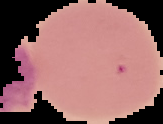
Image is 163×124 pixels. Malaria status: uninfected. The area outside the segmented cell region is set to black. From a thin blood film.